Outline each Plasmodium falciparum-infected red blood cell.
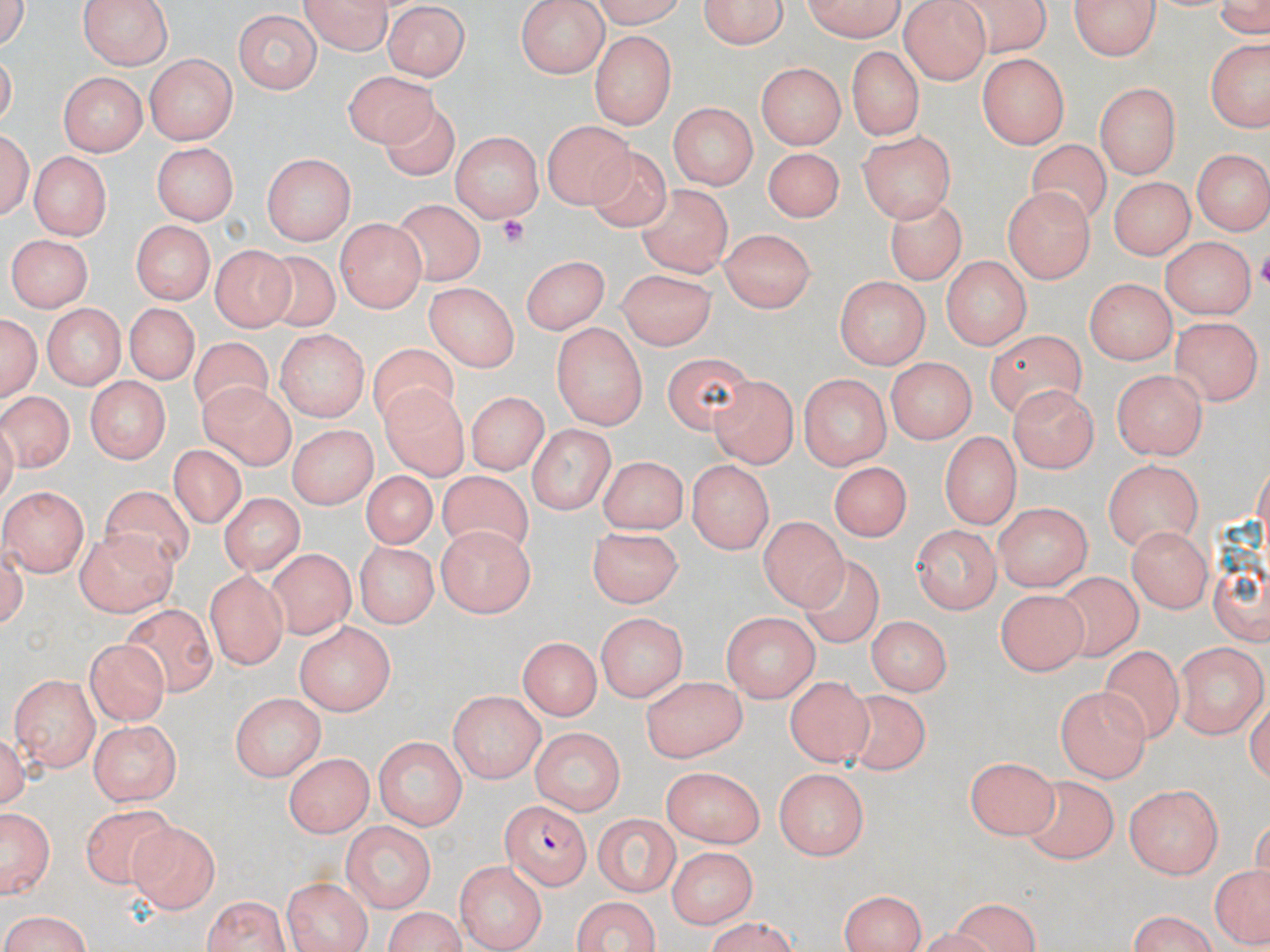
Approximate bounding boxes as named x1/y1/x2/y2 corners in pixels.
Plasmodium falciparum-infected red blood cells: (x1=500, y1=798, x2=590, y2=886).

Uninfected red blood cell locations: (x1=586, y1=0, x2=691, y2=27), (x1=701, y1=0, x2=786, y2=51), (x1=799, y1=0, x2=912, y2=41), (x1=953, y1=0, x2=1055, y2=57), (x1=1072, y1=0, x2=1162, y2=63), (x1=78, y1=1, x2=176, y2=68), (x1=297, y1=1, x2=396, y2=53), (x1=517, y1=1, x2=609, y2=77), (x1=900, y1=1, x2=990, y2=85), (x1=384, y1=5, x2=467, y2=80), (x1=531, y1=9, x2=657, y2=91), (x1=229, y1=10, x2=322, y2=97), (x1=590, y1=32, x2=678, y2=128), (x1=1204, y1=39, x2=1270, y2=133), (x1=846, y1=44, x2=924, y2=140), (x1=145, y1=53, x2=236, y2=143), (x1=977, y1=53, x2=1067, y2=148), (x1=758, y1=61, x2=843, y2=148), (x1=55, y1=70, x2=148, y2=156), (x1=341, y1=70, x2=439, y2=152), (x1=1095, y1=82, x2=1182, y2=174), (x1=377, y1=97, x2=462, y2=179), (x1=669, y1=102, x2=757, y2=192), (x1=543, y1=119, x2=635, y2=208), (x1=858, y1=129, x2=958, y2=222), (x1=449, y1=130, x2=546, y2=220), (x1=1029, y1=140, x2=1111, y2=232), (x1=151, y1=142, x2=238, y2=225), (x1=763, y1=145, x2=845, y2=224), (x1=585, y1=147, x2=676, y2=234), (x1=1189, y1=150, x2=1268, y2=235), (x1=26, y1=151, x2=108, y2=240), (x1=262, y1=152, x2=355, y2=245), (x1=1106, y1=178, x2=1192, y2=264), (x1=637, y1=182, x2=734, y2=279), (x1=1000, y1=186, x2=1096, y2=284), (x1=392, y1=197, x2=487, y2=283), (x1=884, y1=197, x2=967, y2=283), (x1=337, y1=220, x2=426, y2=313), (x1=131, y1=224, x2=210, y2=303), (x1=715, y1=229, x2=819, y2=310), (x1=1160, y1=234, x2=1254, y2=322), (x1=5, y1=235, x2=94, y2=310), (x1=210, y1=246, x2=291, y2=332), (x1=256, y1=250, x2=342, y2=334), (x1=520, y1=254, x2=610, y2=334), (x1=939, y1=256, x2=1033, y2=347), (x1=615, y1=266, x2=718, y2=349), (x1=834, y1=274, x2=930, y2=367), (x1=1086, y1=277, x2=1178, y2=365), (x1=425, y1=283, x2=519, y2=374), (x1=40, y1=303, x2=128, y2=388), (x1=123, y1=304, x2=196, y2=389), (x1=2, y1=312, x2=41, y2=400), (x1=1174, y1=316, x2=1259, y2=406), (x1=551, y1=321, x2=648, y2=427), (x1=275, y1=329, x2=369, y2=424), (x1=982, y1=332, x2=1087, y2=412), (x1=188, y1=340, x2=276, y2=427), (x1=365, y1=344, x2=463, y2=435), (x1=666, y1=349, x2=753, y2=437), (x1=885, y1=358, x2=974, y2=444), (x1=1113, y1=368, x2=1208, y2=458), (x1=708, y1=372, x2=800, y2=469), (x1=800, y1=373, x2=892, y2=468), (x1=85, y1=374, x2=168, y2=461), (x1=199, y1=379, x2=299, y2=471), (x1=381, y1=385, x2=468, y2=479), (x1=1010, y1=385, x2=1101, y2=469), (x1=0, y1=390, x2=75, y2=470), (x1=466, y1=392, x2=544, y2=478), (x1=529, y1=423, x2=615, y2=516), (x1=286, y1=424, x2=378, y2=510), (x1=940, y1=431, x2=1022, y2=524), (x1=168, y1=448, x2=248, y2=535), (x1=596, y1=455, x2=691, y2=531), (x1=1103, y1=458, x2=1205, y2=551), (x1=686, y1=459, x2=777, y2=556), (x1=829, y1=459, x2=913, y2=540), (x1=435, y1=470, x2=532, y2=553), (x1=358, y1=471, x2=438, y2=551), (x1=4, y1=487, x2=86, y2=576), (x1=100, y1=487, x2=193, y2=574), (x1=220, y1=494, x2=303, y2=576), (x1=1210, y1=498, x2=1270, y2=632), (x1=993, y1=500, x2=1093, y2=590), (x1=759, y1=513, x2=849, y2=608), (x1=912, y1=523, x2=1001, y2=613), (x1=1126, y1=525, x2=1211, y2=614), (x1=436, y1=526, x2=536, y2=615), (x1=586, y1=526, x2=688, y2=607), (x1=76, y1=527, x2=177, y2=617), (x1=357, y1=543, x2=434, y2=628), (x1=264, y1=552, x2=357, y2=637), (x1=802, y1=559, x2=880, y2=647), (x1=204, y1=569, x2=291, y2=667), (x1=1049, y1=572, x2=1144, y2=660), (x1=993, y1=584, x2=1085, y2=678), (x1=118, y1=608, x2=220, y2=698), (x1=721, y1=610, x2=817, y2=703), (x1=595, y1=611, x2=686, y2=701), (x1=864, y1=616, x2=954, y2=695), (x1=296, y1=620, x2=395, y2=714), (x1=519, y1=635, x2=598, y2=721), (x1=84, y1=637, x2=168, y2=724), (x1=1176, y1=643, x2=1265, y2=738), (x1=1099, y1=644, x2=1180, y2=745), (x1=482, y1=660, x2=610, y2=741), (x1=10, y1=671, x2=101, y2=766), (x1=638, y1=671, x2=746, y2=761), (x1=784, y1=674, x2=870, y2=768), (x1=1057, y1=686, x2=1150, y2=781), (x1=230, y1=691, x2=323, y2=779), (x1=443, y1=693, x2=543, y2=784), (x1=844, y1=694, x2=932, y2=779), (x1=89, y1=719, x2=183, y2=806), (x1=531, y1=728, x2=625, y2=815), (x1=373, y1=736, x2=467, y2=829), (x1=285, y1=751, x2=374, y2=836), (x1=966, y1=755, x2=1057, y2=839), (x1=772, y1=766, x2=868, y2=859), (x1=659, y1=767, x2=767, y2=849), (x1=1018, y1=774, x2=1119, y2=864), (x1=1125, y1=785, x2=1225, y2=878), (x1=0, y1=803, x2=55, y2=900), (x1=81, y1=808, x2=180, y2=896), (x1=595, y1=810, x2=681, y2=894), (x1=126, y1=820, x2=224, y2=910), (x1=342, y1=821, x2=434, y2=913), (x1=668, y1=845, x2=757, y2=930), (x1=452, y1=856, x2=549, y2=947), (x1=1205, y1=863, x2=1270, y2=945), (x1=282, y1=874, x2=372, y2=952), (x1=836, y1=887, x2=927, y2=952), (x1=198, y1=895, x2=294, y2=952), (x1=568, y1=897, x2=667, y2=952), (x1=949, y1=900, x2=1039, y2=952), (x1=378, y1=908, x2=469, y2=952), (x1=0, y1=911, x2=97, y2=952), (x1=1122, y1=913, x2=1223, y2=951), (x1=699, y1=920, x2=804, y2=950). Platelet locations: (x1=500, y1=213, x2=529, y2=243). Slide-level diagnosis: Plasmodium falciparum. May-Grünwald-Giemsa-stained preparation. Light microscopy. 1000x magnification. Single field of view. Image is 1270×952 pixels. Thin blood film.